Outline each blood parasite and name the species.
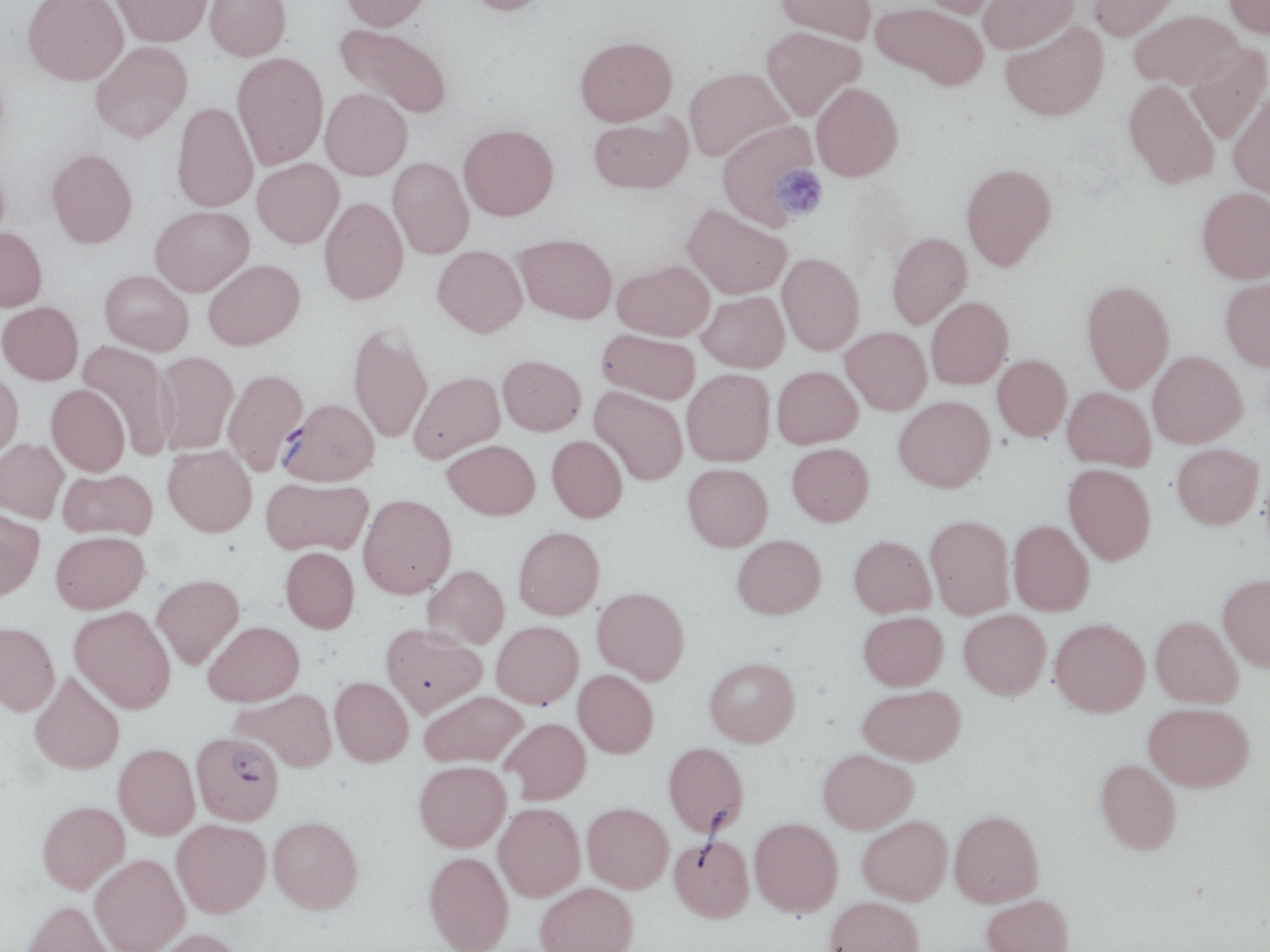

Approximate bounding boxes as (x1, y1, x2, y2) in pixels.
Plasmodium falciparum-infected red blood cells: (278, 397, 379, 486), (190, 731, 284, 825).
No Plasmodium ovale, Plasmodium malariae, Plasmodium vivax, Babesia divergens, or Trypanosoma brucei observed.

slide_level_diagnosis: Plasmodium falciparum
preparation: thin blood smear
uninfected_red_blood_cell_locations: 'approximate bounding boxes as (x1, y1, x2, y2) in pixels: (22, 0, 128, 86), (109, 0, 212, 47), (204, 0, 291, 61), (340, 0, 431, 32), (460, 0, 551, 15), (774, 0, 876, 43), (914, 0, 1003, 19), (977, 0, 1078, 54), (1087, 0, 1181, 41), (1224, 0, 1270, 39), (870, 2, 987, 90), (1130, 9, 1242, 89), (1000, 20, 1109, 121), (335, 23, 452, 119), (761, 26, 865, 120), (575, 35, 677, 126), (90, 41, 192, 143), (1185, 43, 1270, 143), (232, 52, 328, 170), (684, 67, 793, 162), (1123, 79, 1220, 189), (810, 82, 903, 181), (320, 88, 412, 179), (1228, 92, 1270, 200), (171, 102, 258, 212), (588, 113, 692, 194), (715, 120, 824, 232), (458, 123, 558, 220), (46, 147, 138, 249), (387, 157, 474, 259), (251, 158, 343, 248), (961, 163, 1057, 271), (1196, 187, 1270, 284), (319, 197, 408, 305), (682, 204, 791, 299), (150, 206, 253, 297), (0, 227, 47, 312), (886, 232, 972, 329), (513, 233, 617, 323), (432, 245, 527, 337), (777, 252, 864, 355), (203, 259, 305, 351), (612, 259, 714, 341), (99, 270, 194, 356), (1220, 275, 1270, 370), (1081, 280, 1174, 393), (696, 291, 789, 372), (926, 296, 1013, 388), (0, 301, 83, 385), (347, 321, 433, 443), (841, 326, 931, 414), (597, 328, 700, 404), (77, 339, 175, 460), (1148, 350, 1247, 448), (154, 351, 238, 456), (497, 354, 586, 435), (992, 354, 1071, 441), (772, 365, 862, 448), (222, 368, 308, 477), (682, 368, 775, 466), (0, 370, 23, 462), (408, 371, 504, 462), (46, 384, 129, 475), (590, 387, 688, 485), (1063, 387, 1155, 470), (893, 396, 995, 492), (547, 435, 627, 522), (0, 438, 69, 523), (442, 440, 540, 519), (787, 442, 874, 526), (1171, 443, 1262, 529), (162, 445, 257, 537), (1063, 463, 1156, 565), (682, 464, 772, 551), (58, 468, 156, 539), (261, 477, 371, 555), (358, 493, 456, 598), (0, 507, 44, 601), (925, 515, 1014, 619), (1008, 519, 1095, 616), (513, 526, 604, 619), (51, 531, 149, 613), (732, 534, 826, 619), (848, 535, 936, 617), (280, 547, 359, 632), (422, 565, 509, 649), (151, 574, 244, 668), (1218, 574, 1270, 672), (593, 586, 690, 684), (69, 605, 175, 713), (959, 609, 1051, 698), (858, 611, 948, 690), (1151, 616, 1243, 707), (1050, 618, 1149, 716), (203, 620, 304, 706), (491, 620, 583, 708), (0, 622, 59, 715), (380, 624, 486, 716), (704, 657, 800, 747), (574, 669, 658, 757), (29, 671, 124, 774), (329, 676, 413, 766), (858, 684, 965, 765), (230, 689, 337, 772), (418, 690, 527, 767), (1144, 702, 1255, 791), (500, 717, 591, 804), (662, 741, 750, 837), (113, 743, 200, 839), (817, 749, 918, 833), (1095, 758, 1182, 854), (414, 761, 511, 851), (37, 800, 129, 893), (582, 802, 673, 892), (494, 803, 585, 901), (949, 810, 1044, 907), (268, 815, 363, 913), (858, 816, 952, 905), (750, 817, 843, 916), (172, 819, 271, 917), (668, 833, 755, 922), (423, 851, 513, 951), (90, 854, 189, 952), (535, 882, 638, 952), (982, 894, 1074, 952), (825, 896, 925, 952), (21, 900, 117, 952), (148, 928, 245, 952)'
modality: optical microscopy
field_of_view: one of a larger specimen
platelet_locations: 'approximate bounding boxes as (x1, y1, x2, y2) in pixels: (773, 165, 827, 221)'
stain: May-Grünwald-Giemsa
image_size: 1270×952 pixels
magnification: 1000x